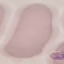
Summary:
  - Result: no malaria parasites seen
  - Preparation: thin blood smear
  - Stain: Giemsa
  - Capture: smartphone camera at the microscope eyepiece
  - Image type: automatically extracted cell patch, resized to 64 × 64 pixels